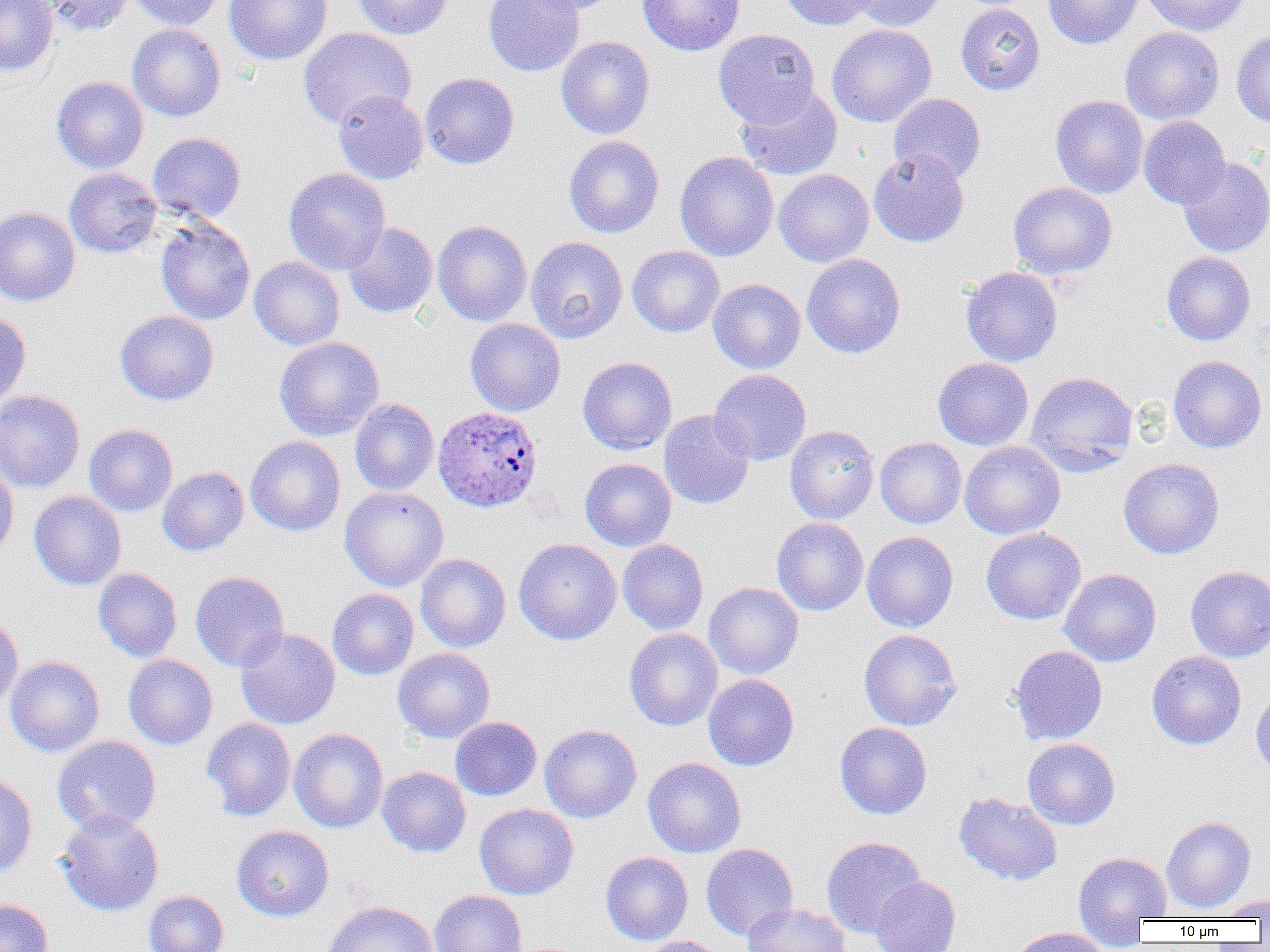
slide-level diagnosis = Plasmodium ovale
magnification = 1000x
modality = light microscopy
uninfected red blood cell locations = approximate bounding boxes as named x1/y1/x2/y2 corners in pixels: (x1=0, y1=0, x2=58, y2=77), (x1=39, y1=0, x2=135, y2=37), (x1=128, y1=0, x2=227, y2=30), (x1=224, y1=0, x2=332, y2=65), (x1=352, y1=0, x2=453, y2=39), (x1=483, y1=0, x2=585, y2=77), (x1=517, y1=0, x2=624, y2=16), (x1=637, y1=0, x2=745, y2=56), (x1=779, y1=0, x2=877, y2=30), (x1=850, y1=0, x2=947, y2=31), (x1=1042, y1=0, x2=1144, y2=49), (x1=1141, y1=0, x2=1251, y2=36), (x1=955, y1=3, x2=1046, y2=95), (x1=127, y1=23, x2=226, y2=122), (x1=827, y1=24, x2=937, y2=127), (x1=1119, y1=26, x2=1225, y2=125), (x1=298, y1=27, x2=416, y2=129), (x1=1231, y1=28, x2=1270, y2=128), (x1=713, y1=29, x2=820, y2=127), (x1=555, y1=35, x2=655, y2=139), (x1=420, y1=72, x2=520, y2=169), (x1=50, y1=76, x2=149, y2=174), (x1=735, y1=83, x2=843, y2=181), (x1=333, y1=89, x2=429, y2=184), (x1=889, y1=92, x2=986, y2=183), (x1=1050, y1=94, x2=1149, y2=199), (x1=1138, y1=116, x2=1230, y2=209), (x1=147, y1=132, x2=246, y2=223), (x1=564, y1=135, x2=665, y2=238), (x1=868, y1=148, x2=970, y2=247), (x1=674, y1=151, x2=779, y2=262), (x1=1177, y1=157, x2=1270, y2=258), (x1=63, y1=167, x2=162, y2=259), (x1=283, y1=168, x2=390, y2=275), (x1=773, y1=169, x2=874, y2=268), (x1=1008, y1=181, x2=1117, y2=279), (x1=0, y1=206, x2=80, y2=307), (x1=155, y1=218, x2=255, y2=325), (x1=432, y1=220, x2=532, y2=326), (x1=342, y1=222, x2=438, y2=318), (x1=525, y1=236, x2=628, y2=344), (x1=627, y1=245, x2=725, y2=338), (x1=1161, y1=251, x2=1256, y2=346), (x1=801, y1=253, x2=905, y2=358), (x1=249, y1=257, x2=345, y2=351), (x1=961, y1=266, x2=1063, y2=367), (x1=708, y1=278, x2=806, y2=374), (x1=114, y1=310, x2=219, y2=406), (x1=0, y1=311, x2=31, y2=412), (x1=465, y1=318, x2=565, y2=416), (x1=274, y1=336, x2=385, y2=441), (x1=1168, y1=354, x2=1268, y2=453), (x1=577, y1=356, x2=677, y2=455), (x1=932, y1=357, x2=1033, y2=451), (x1=709, y1=369, x2=811, y2=465), (x1=1025, y1=371, x2=1139, y2=476), (x1=0, y1=390, x2=86, y2=494), (x1=350, y1=398, x2=439, y2=496), (x1=658, y1=409, x2=756, y2=509), (x1=83, y1=424, x2=178, y2=516), (x1=784, y1=424, x2=880, y2=524), (x1=245, y1=436, x2=346, y2=537), (x1=875, y1=437, x2=966, y2=528), (x1=959, y1=441, x2=1065, y2=540), (x1=1118, y1=457, x2=1224, y2=559), (x1=579, y1=458, x2=677, y2=551), (x1=0, y1=460, x2=19, y2=562), (x1=157, y1=466, x2=249, y2=556), (x1=339, y1=486, x2=448, y2=591), (x1=29, y1=491, x2=127, y2=590), (x1=771, y1=517, x2=869, y2=616), (x1=980, y1=527, x2=1086, y2=625), (x1=862, y1=531, x2=959, y2=632), (x1=513, y1=538, x2=622, y2=645), (x1=617, y1=539, x2=708, y2=635), (x1=415, y1=553, x2=511, y2=652), (x1=1185, y1=565, x2=1270, y2=662), (x1=92, y1=568, x2=183, y2=662), (x1=1059, y1=568, x2=1162, y2=667), (x1=189, y1=571, x2=290, y2=672), (x1=704, y1=582, x2=804, y2=679), (x1=327, y1=588, x2=419, y2=680), (x1=0, y1=614, x2=24, y2=712), (x1=235, y1=627, x2=340, y2=729), (x1=624, y1=628, x2=723, y2=731), (x1=859, y1=629, x2=962, y2=731), (x1=1010, y1=645, x2=1107, y2=745), (x1=392, y1=647, x2=495, y2=744), (x1=1146, y1=651, x2=1246, y2=750), (x1=123, y1=654, x2=218, y2=750), (x1=5, y1=655, x2=105, y2=757), (x1=702, y1=674, x2=799, y2=771), (x1=1250, y1=684, x2=1270, y2=779), (x1=450, y1=716, x2=542, y2=801), (x1=201, y1=717, x2=296, y2=821), (x1=834, y1=722, x2=932, y2=819), (x1=539, y1=724, x2=642, y2=823), (x1=289, y1=728, x2=389, y2=833), (x1=52, y1=735, x2=161, y2=835), (x1=1022, y1=738, x2=1120, y2=829), (x1=643, y1=757, x2=746, y2=858), (x1=376, y1=766, x2=471, y2=857), (x1=0, y1=771, x2=38, y2=878), (x1=953, y1=791, x2=1062, y2=887), (x1=474, y1=803, x2=579, y2=900), (x1=55, y1=809, x2=164, y2=917), (x1=1161, y1=816, x2=1256, y2=913), (x1=231, y1=825, x2=334, y2=922), (x1=821, y1=836, x2=926, y2=937), (x1=700, y1=843, x2=798, y2=941), (x1=1073, y1=851, x2=1172, y2=931), (x1=600, y1=852, x2=693, y2=944), (x1=869, y1=876, x2=961, y2=952), (x1=143, y1=890, x2=229, y2=952), (x1=429, y1=890, x2=527, y2=952), (x1=1212, y1=895, x2=1270, y2=920), (x1=0, y1=898, x2=54, y2=952), (x1=321, y1=900, x2=439, y2=952), (x1=741, y1=903, x2=851, y2=952), (x1=1008, y1=927, x2=1112, y2=952), (x1=635, y1=936, x2=727, y2=952)
preparation = thin blood smear
field of view = single
Plasmodium ovale-infected red blood cell locations = approximate bounding boxes as named x1/y1/x2/y2 corners in pixels: (x1=433, y1=406, x2=543, y2=512)
image size = 1270×952 pixels